Outline each blood parasite and name the species.
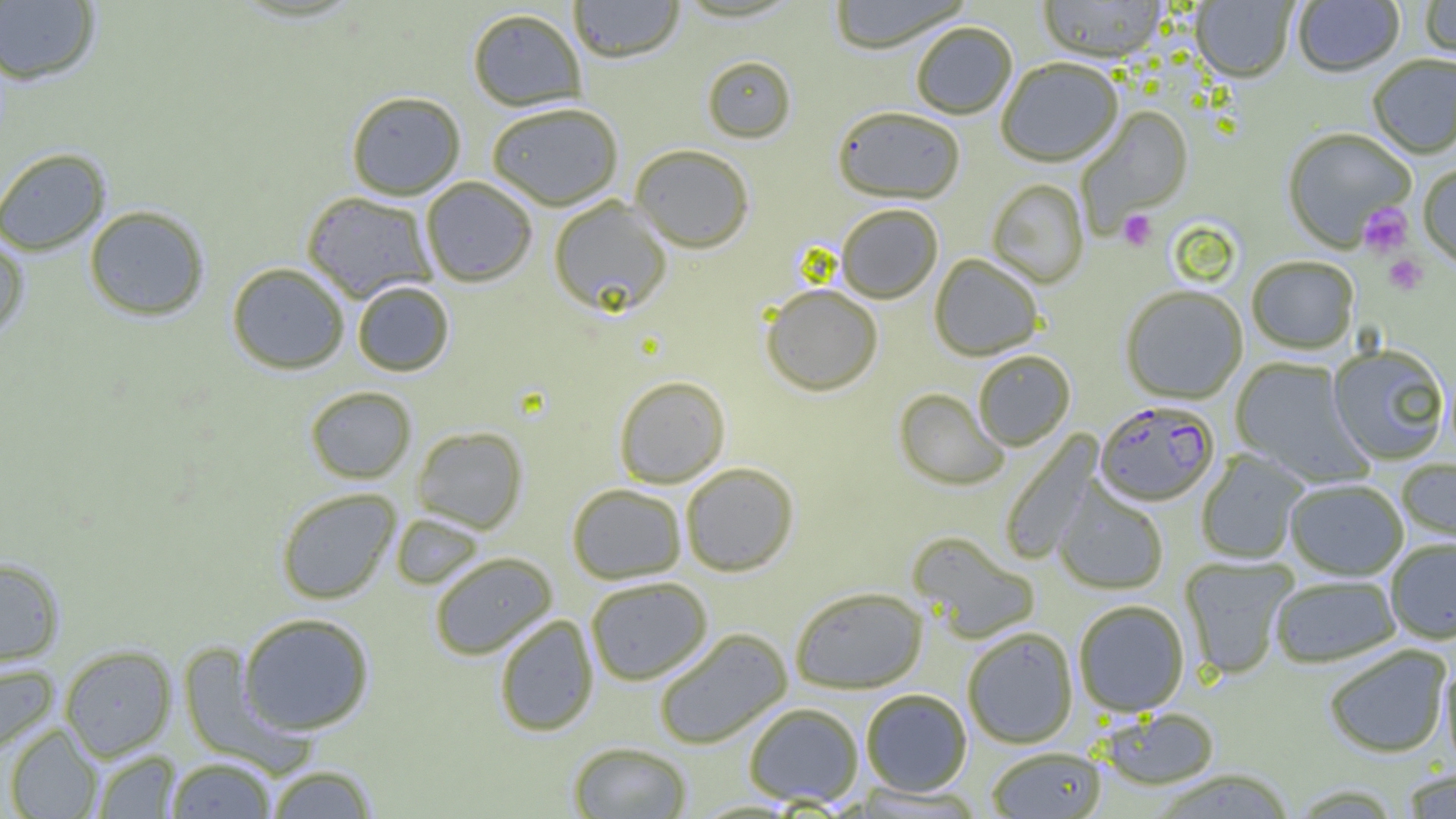
Approximate bounding boxes as (x1, y1, x2, y2) in pixels.
Plasmodium falciparum-infected red blood cells: (1095, 403, 1219, 508).
No Plasmodium ovale, Plasmodium malariae, Plasmodium vivax, Babesia divergens, or Trypanosoma brucei observed.

slide-level diagnosis = Plasmodium falciparum
field of view = one of a larger specimen
preparation = thin blood smear
platelet locations = approximate bounding boxes as (x1, y1, x2, y2) in pixels: (1358, 204, 1412, 257), (1118, 210, 1156, 250), (1384, 253, 1428, 294)
modality = light microscopy
uninfected red blood cell locations = approximate bounding boxes as (x1, y1, x2, y2) in pixels: (569, 0, 684, 63), (827, 0, 972, 55), (1038, 0, 1167, 65), (1293, 0, 1404, 79), (1420, 0, 1456, 64), (0, 1, 101, 85), (1191, 1, 1297, 84), (467, 8, 587, 111), (911, 24, 1017, 120), (1368, 56, 1456, 160), (702, 57, 796, 144), (997, 60, 1123, 168), (346, 91, 466, 200), (486, 102, 623, 210), (1076, 106, 1193, 232), (832, 109, 965, 206), (1282, 130, 1416, 253), (630, 145, 754, 254), (0, 147, 111, 256), (1418, 166, 1456, 273), (421, 176, 537, 287), (986, 180, 1089, 289), (300, 191, 438, 302), (548, 196, 673, 317), (83, 205, 210, 321), (836, 206, 942, 304), (0, 236, 29, 339), (929, 255, 1043, 361), (1247, 257, 1358, 355), (227, 262, 349, 374), (352, 281, 454, 376), (761, 285, 883, 397), (1120, 287, 1247, 405), (1328, 346, 1449, 465), (973, 352, 1075, 451), (1230, 358, 1372, 488), (613, 376, 730, 488), (305, 385, 417, 483), (894, 389, 1008, 491), (411, 426, 528, 533), (1000, 431, 1104, 565), (1196, 450, 1309, 564), (1397, 458, 1456, 546), (680, 463, 799, 576), (1052, 479, 1168, 595), (1286, 480, 1408, 581), (567, 483, 686, 584), (276, 487, 401, 604), (390, 513, 485, 590), (907, 531, 1040, 644), (1385, 539, 1456, 645), (429, 552, 557, 660), (1180, 556, 1297, 680), (0, 558, 65, 668), (585, 576, 713, 685), (1270, 576, 1400, 668), (789, 586, 928, 694), (1073, 600, 1189, 717), (238, 612, 375, 735), (493, 614, 599, 736), (962, 627, 1078, 748), (653, 628, 792, 749), (177, 642, 309, 773), (59, 644, 177, 761), (1324, 645, 1452, 758), (1440, 659, 1456, 776), (0, 662, 58, 755), (860, 688, 972, 796), (743, 702, 864, 807), (1099, 708, 1220, 791), (5, 723, 102, 819), (567, 741, 692, 819), (986, 747, 1106, 818), (91, 750, 180, 818), (165, 757, 277, 818), (264, 764, 379, 818), (1400, 768, 1456, 818), (1149, 769, 1297, 818)
image size = 1456×819 pixels
magnification = 1000x